Outline each Plasmodium falciparum-infected red blood cell.
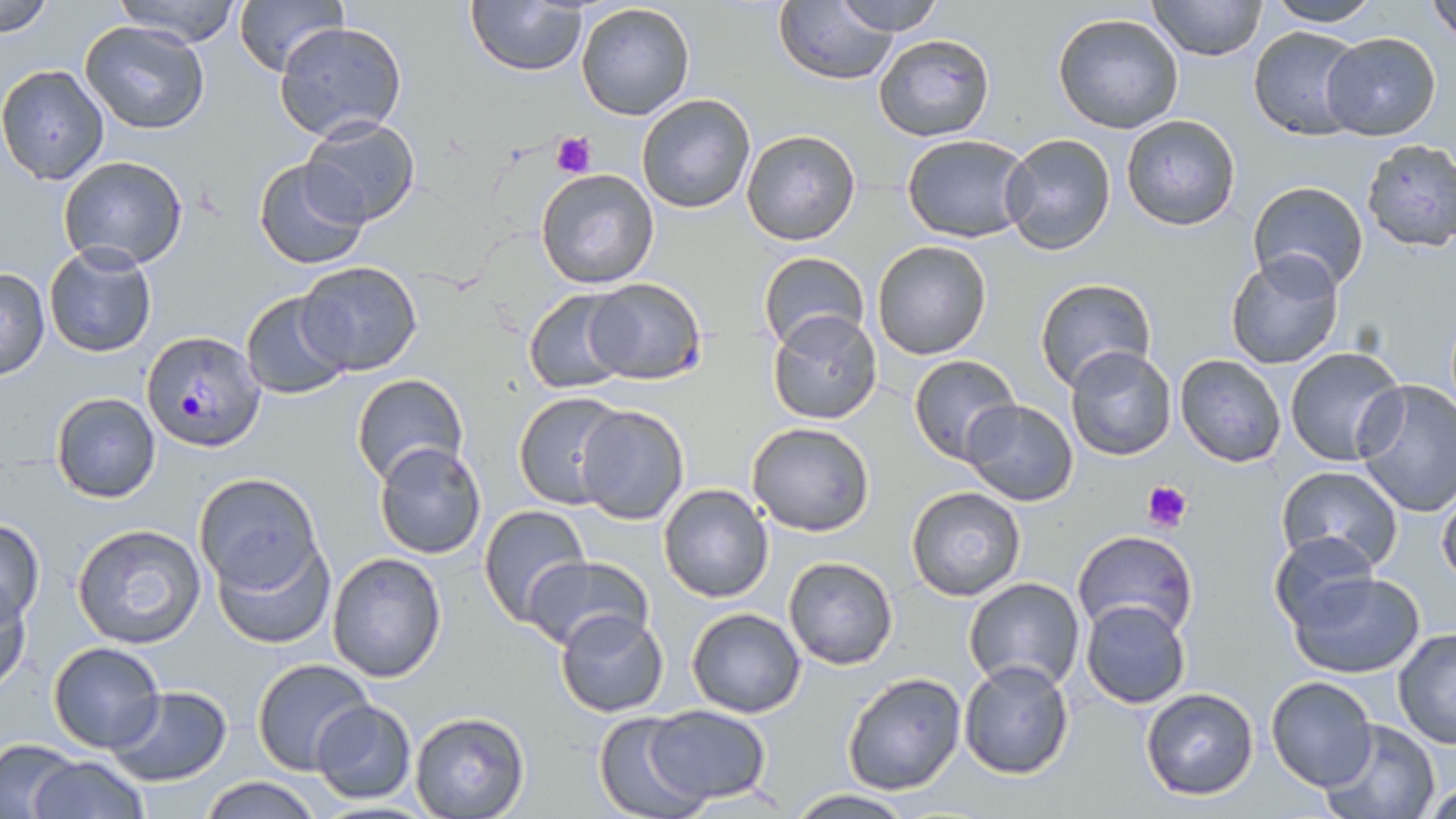
Approximate bounding boxes as (x1,y1)-(x2,y2) corner pairs in pixels.
Plasmodium falciparum-infected red blood cells: (142,331)-(266,451).

Summary:
  - Uninfected red blood cell locations: (1,0)-(56,36), (108,0)-(245,46), (233,0)-(348,76), (466,0)-(590,75), (831,0)-(948,36), (1148,0)-(1267,63), (1426,0)-(1456,43), (576,1)-(696,121), (1260,1)-(1382,28), (775,4)-(899,85), (1052,13)-(1186,135), (79,19)-(209,135), (275,21)-(407,141), (1247,25)-(1367,141), (873,32)-(996,143), (1319,33)-(1442,140), (0,63)-(109,185), (635,93)-(756,214), (1121,113)-(1240,232), (300,115)-(422,227), (739,128)-(862,247), (1000,133)-(1117,256), (899,134)-(1034,243), (1359,137)-(1456,253), (58,156)-(189,271), (254,157)-(372,270), (535,168)-(659,288), (1245,182)-(1369,296), (871,240)-(992,360), (43,243)-(157,360), (758,251)-(869,353), (1223,251)-(1346,371), (293,260)-(423,376), (0,267)-(49,380), (1032,277)-(1155,393), (580,278)-(708,384), (522,288)-(634,394), (239,290)-(356,402), (766,311)-(883,426), (1282,345)-(1407,467), (1065,347)-(1178,461), (908,354)-(1021,464), (1174,354)-(1288,469), (351,374)-(468,488), (1354,380)-(1456,516), (49,392)-(161,503), (512,392)-(628,508), (961,398)-(1080,507), (574,404)-(689,524), (746,420)-(875,535), (373,441)-(488,559), (1275,466)-(1403,573), (193,473)-(325,593), (658,483)-(774,602), (1435,483)-(1456,589), (905,486)-(1028,602), (478,503)-(589,623), (0,518)-(45,625), (70,523)-(207,650), (1071,530)-(1198,639), (1270,530)-(1380,631), (214,536)-(335,648), (327,552)-(448,682), (524,555)-(655,655), (783,556)-(898,670), (1287,571)-(1428,676), (963,577)-(1087,694), (0,581)-(32,695), (1080,599)-(1192,709), (685,607)-(807,718), (553,609)-(670,717), (1392,627)-(1456,751), (45,642)-(165,753), (251,657)-(376,775), (956,659)-(1074,780), (841,671)-(966,794), (1266,675)-(1378,791), (105,684)-(234,787), (1139,687)-(1260,801), (311,700)-(417,803), (646,704)-(771,805), (593,711)-(709,819), (408,712)-(530,819), (1317,718)-(1441,819), (1,739)-(78,816), (26,755)-(148,819), (200,776)-(325,818), (1423,777)-(1454,816), (786,789)-(919,818)
  - Platelet locations: (552,132)-(595,178), (1142,480)-(1192,532)
  - Slide-level diagnosis: Plasmodium falciparum
  - Field of view: single
  - Magnification: 1000x
  - Preparation: thin blood film
  - Modality: light microscopy
  - Stain: May-Grünwald-Giemsa
  - Image size: 1456×819 pixels